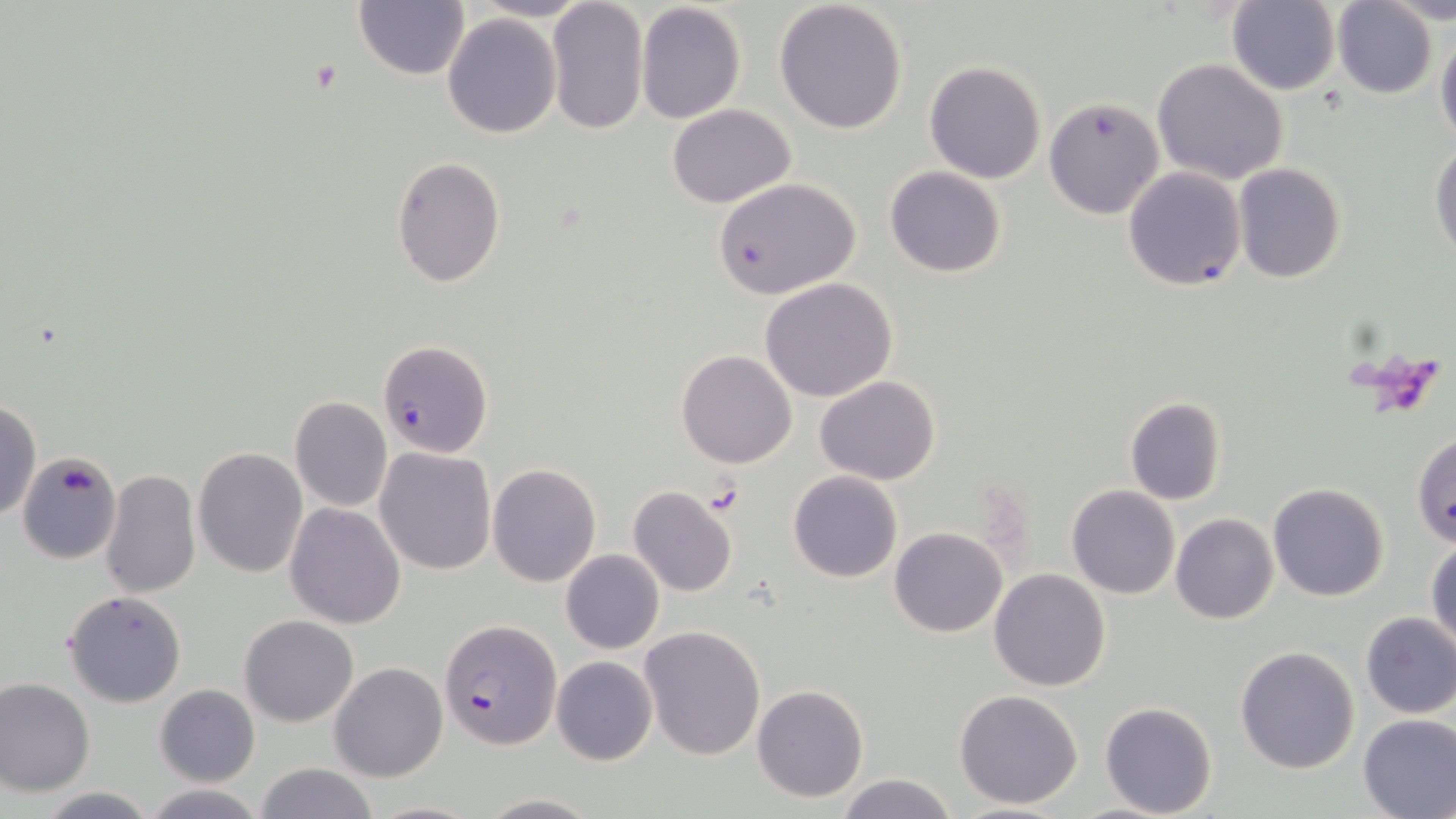
Approximate bounding boxes as named x1/y1/x2/y2 corners in pixels. Plasmodium falciparum-infected red blood cell locations: (x1=377, y1=340, x2=493, y2=460), (x1=440, y1=620, x2=560, y2=749). Uninfected red blood cell locations: (x1=773, y1=0, x2=909, y2=135), (x1=471, y1=1, x2=595, y2=23), (x1=1334, y1=1, x2=1438, y2=99), (x1=354, y1=2, x2=469, y2=80), (x1=635, y1=2, x2=747, y2=124), (x1=1226, y1=2, x2=1342, y2=95), (x1=546, y1=3, x2=650, y2=133), (x1=441, y1=13, x2=562, y2=138), (x1=1435, y1=30, x2=1456, y2=149), (x1=1152, y1=58, x2=1289, y2=185), (x1=924, y1=60, x2=1047, y2=184), (x1=1045, y1=96, x2=1165, y2=219), (x1=667, y1=104, x2=797, y2=208), (x1=1428, y1=142, x2=1455, y2=260), (x1=392, y1=158, x2=505, y2=286), (x1=1122, y1=165, x2=1247, y2=291), (x1=1232, y1=165, x2=1346, y2=283), (x1=884, y1=166, x2=1007, y2=278), (x1=712, y1=177, x2=862, y2=297), (x1=757, y1=278, x2=899, y2=402), (x1=677, y1=349, x2=799, y2=468), (x1=814, y1=375, x2=941, y2=486), (x1=288, y1=397, x2=393, y2=511), (x1=1124, y1=397, x2=1227, y2=506), (x1=0, y1=399, x2=41, y2=523), (x1=1411, y1=432, x2=1455, y2=545), (x1=191, y1=446, x2=309, y2=579), (x1=373, y1=447, x2=497, y2=575), (x1=17, y1=452, x2=123, y2=566), (x1=487, y1=462, x2=600, y2=587), (x1=100, y1=469, x2=202, y2=599), (x1=787, y1=471, x2=903, y2=583), (x1=1268, y1=483, x2=1391, y2=602), (x1=627, y1=485, x2=739, y2=598), (x1=1067, y1=485, x2=1181, y2=599), (x1=284, y1=502, x2=408, y2=629), (x1=1170, y1=513, x2=1279, y2=624), (x1=890, y1=527, x2=1008, y2=638), (x1=1428, y1=537, x2=1456, y2=651), (x1=560, y1=550, x2=665, y2=654), (x1=989, y1=569, x2=1111, y2=692), (x1=63, y1=590, x2=187, y2=707), (x1=1359, y1=612, x2=1456, y2=718), (x1=238, y1=614, x2=359, y2=728), (x1=639, y1=626, x2=766, y2=760), (x1=1235, y1=645, x2=1361, y2=774), (x1=551, y1=655, x2=657, y2=766), (x1=330, y1=662, x2=448, y2=783), (x1=0, y1=677, x2=95, y2=796), (x1=154, y1=684, x2=259, y2=787), (x1=752, y1=684, x2=868, y2=802), (x1=954, y1=689, x2=1084, y2=810), (x1=1100, y1=702, x2=1218, y2=818), (x1=1357, y1=713, x2=1456, y2=819), (x1=252, y1=762, x2=380, y2=819), (x1=837, y1=773, x2=957, y2=818), (x1=140, y1=784, x2=268, y2=819), (x1=30, y1=786, x2=163, y2=818), (x1=475, y1=793, x2=603, y2=818). Platelet locations: (x1=701, y1=484, x2=745, y2=515). Slide-level diagnosis: Plasmodium falciparum. May-Grünwald-Giemsa-stained preparation. Thin blood smear. Optical microscopy. Image is 1456×819 pixels. Captured at 1000x magnification. Single field of view.